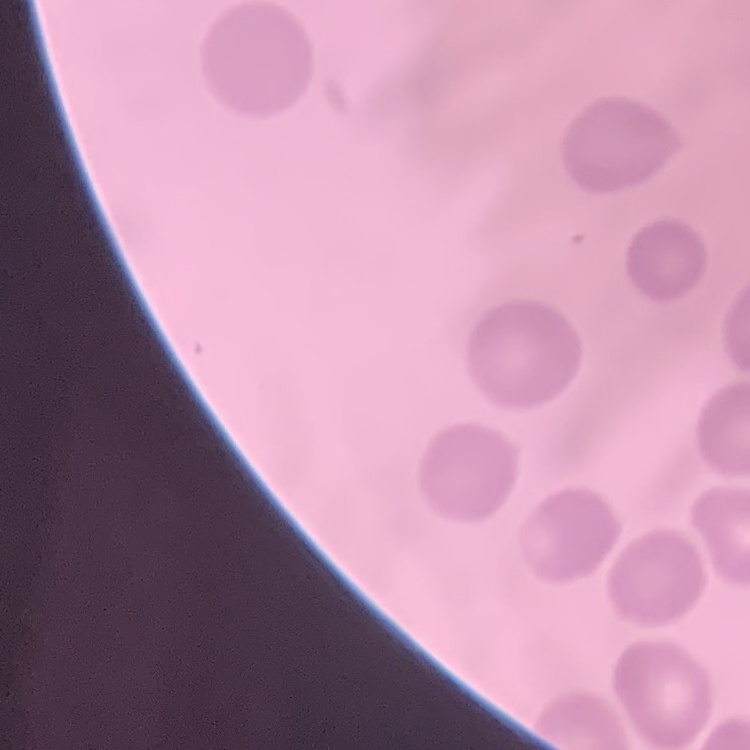
{
  "red_blood_cell_morphology": "no rouleaux formation",
  "preparation": "thin peripheral smear",
  "stain": "Field's or Giemsa",
  "image_type": "one tile cut from a larger photomicrograph"
}